Mark where platelets are.
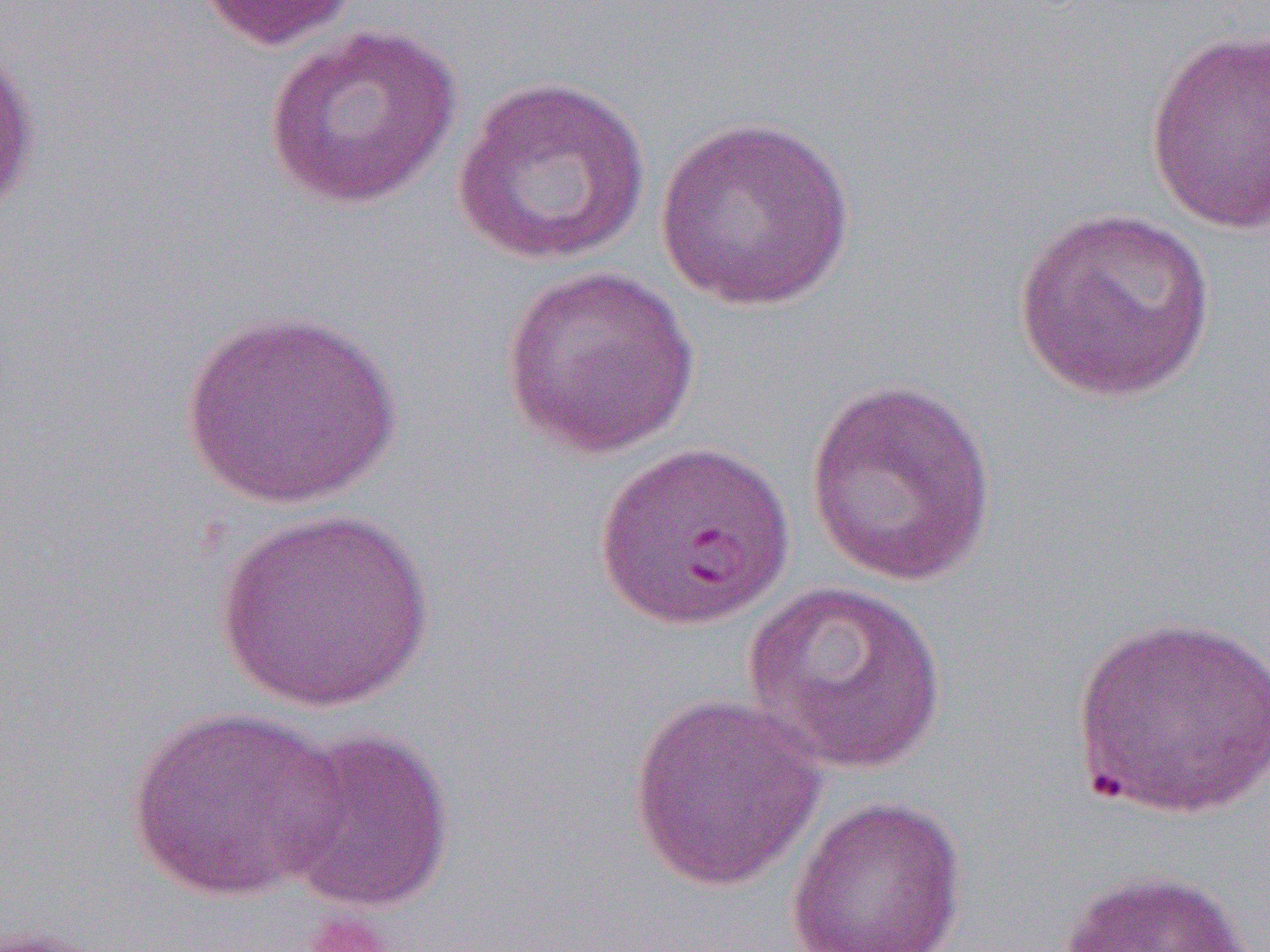
Approximate bounding boxes as [x1, y1, x2, y2] in pixels.
Platelets: [298, 909, 397, 952].

slide-level diagnosis = Plasmodium falciparum
preparation = thin blood smear
field of view = single
modality = optical microscopy
uninfected red blood cell locations = approximate bounding boxes as [x1, y1, x2, y2] in pixels: [194, 0, 363, 53], [263, 25, 461, 210], [1143, 27, 1270, 235], [0, 37, 42, 220], [452, 75, 650, 267], [654, 116, 858, 312], [1012, 206, 1220, 403], [499, 263, 701, 459], [176, 307, 405, 510], [805, 379, 998, 587], [592, 440, 795, 629], [211, 507, 438, 713], [744, 580, 948, 775], [1071, 612, 1270, 819], [626, 692, 827, 893], [123, 706, 349, 903], [277, 725, 456, 914], [785, 796, 968, 952], [1058, 867, 1257, 952], [0, 923, 112, 952]
magnification = 1000x
image size = 1270×952 pixels